Outline each Plasmodium falciparum-infected red blood cell.
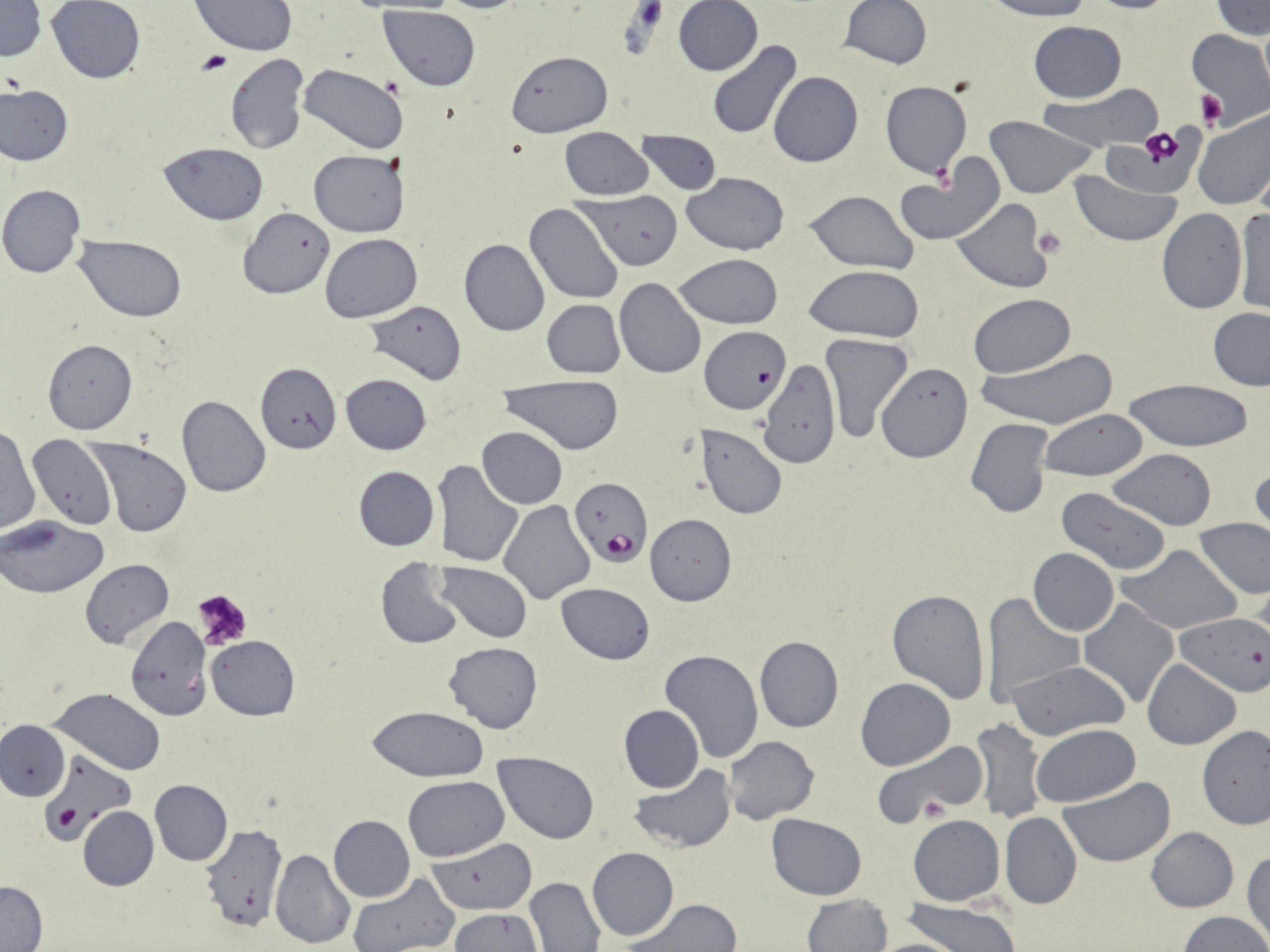

Approximate bounding boxes as [x1, y1, x2, y2] in pixels.
Plasmodium falciparum-infected red blood cells (subset): [568, 477, 651, 567].

Uninfected red blood cell locations (subset): [428, 0, 534, 14], [840, 0, 931, 70], [983, 0, 1096, 21], [1083, 0, 1182, 14], [1210, 0, 1269, 39], [0, 1, 44, 61], [47, 1, 145, 84], [191, 1, 297, 57], [673, 1, 762, 76], [380, 6, 482, 91], [1028, 21, 1126, 102], [1187, 29, 1269, 124], [706, 42, 802, 140], [506, 49, 613, 136], [224, 53, 308, 155], [298, 63, 409, 154], [768, 71, 862, 168], [880, 81, 972, 178], [1, 84, 72, 166], [1042, 86, 1166, 152], [1193, 111, 1270, 211], [984, 116, 1098, 197], [560, 127, 654, 200], [637, 130, 723, 195], [159, 142, 269, 225], [308, 150, 409, 237], [895, 156, 1005, 247], [1070, 170, 1181, 246], [681, 172, 790, 255], [0, 184, 86, 279], [803, 189, 920, 273], [578, 192, 683, 271], [951, 200, 1049, 293], [526, 205, 624, 305], [239, 206, 335, 300], [1233, 207, 1269, 316], [1156, 210, 1246, 313], [320, 233, 422, 323], [75, 234, 188, 321], [459, 239, 550, 336], [675, 253, 784, 328], [803, 265, 923, 342], [614, 277, 705, 379], [970, 294, 1076, 377], [366, 300, 467, 386], [542, 300, 624, 378], [1207, 308, 1270, 390], [701, 325, 791, 416], [822, 333, 913, 442], [42, 339, 138, 435], [975, 348, 1119, 432], [758, 359, 839, 467], [255, 363, 338, 453], [877, 363, 973, 461], [340, 374, 431, 455], [496, 375, 628, 454], [1123, 378, 1254, 450], [176, 394, 271, 497], [1040, 409, 1149, 482], [966, 418, 1053, 519], [476, 427, 569, 508], [0, 428, 40, 535], [28, 436, 117, 529], [85, 439, 194, 537], [1107, 449, 1216, 530], [435, 461, 524, 567], [1249, 464, 1269, 541], [353, 466, 440, 550], [1056, 487, 1170, 576], [500, 501, 595, 603], [645, 514, 738, 605], [0, 515, 110, 598], [1194, 519, 1270, 599], [1118, 544, 1240, 635], [1028, 548, 1118, 636], [375, 557, 465, 649], [80, 559, 174, 648], [435, 561, 532, 642], [556, 584, 655, 664], [886, 588, 992, 702], [980, 593, 1084, 710], [1078, 599, 1180, 710], [1176, 614, 1269, 697], [124, 615, 211, 720], [207, 636, 300, 720], [754, 636, 843, 733], [443, 641, 544, 733], [657, 648, 763, 765], [1143, 659, 1241, 749], [1006, 660, 1131, 740], [855, 678, 956, 771], [51, 687, 166, 775], [619, 705, 704, 793], [368, 706, 489, 782], [972, 719, 1045, 826], [0, 721, 69, 801], [1031, 723, 1141, 807], [1197, 725, 1270, 828], [723, 736, 819, 824], [870, 738, 987, 827], [493, 751, 600, 844], [630, 765, 737, 853], [402, 776, 507, 862], [1060, 778, 1176, 866], [150, 779, 233, 866], [78, 806, 158, 891], [1000, 813, 1081, 909], [766, 814, 865, 900], [908, 814, 1005, 907], [328, 815, 414, 902], [198, 826, 288, 933], [1146, 827, 1239, 912], [429, 838, 536, 915], [587, 846, 679, 941], [270, 849, 356, 949], [1244, 849, 1270, 944], [347, 873, 459, 952], [525, 877, 604, 951], [1, 878, 48, 950], [802, 894, 893, 952], [625, 899, 742, 951], [898, 899, 1020, 952], [451, 910, 544, 952], [1177, 910, 1269, 952]. Platelet locations: [198, 50, 231, 76], [1198, 90, 1225, 129], [1136, 126, 1188, 169], [1032, 227, 1066, 259], [194, 591, 253, 652]. Slide-level diagnosis: Plasmodium falciparum. Optical microscopy. One field of a larger specimen. Thin blood smear. Captured at 1000x magnification. Image is 1270×952 pixels. May-Grünwald-Giemsa stain.